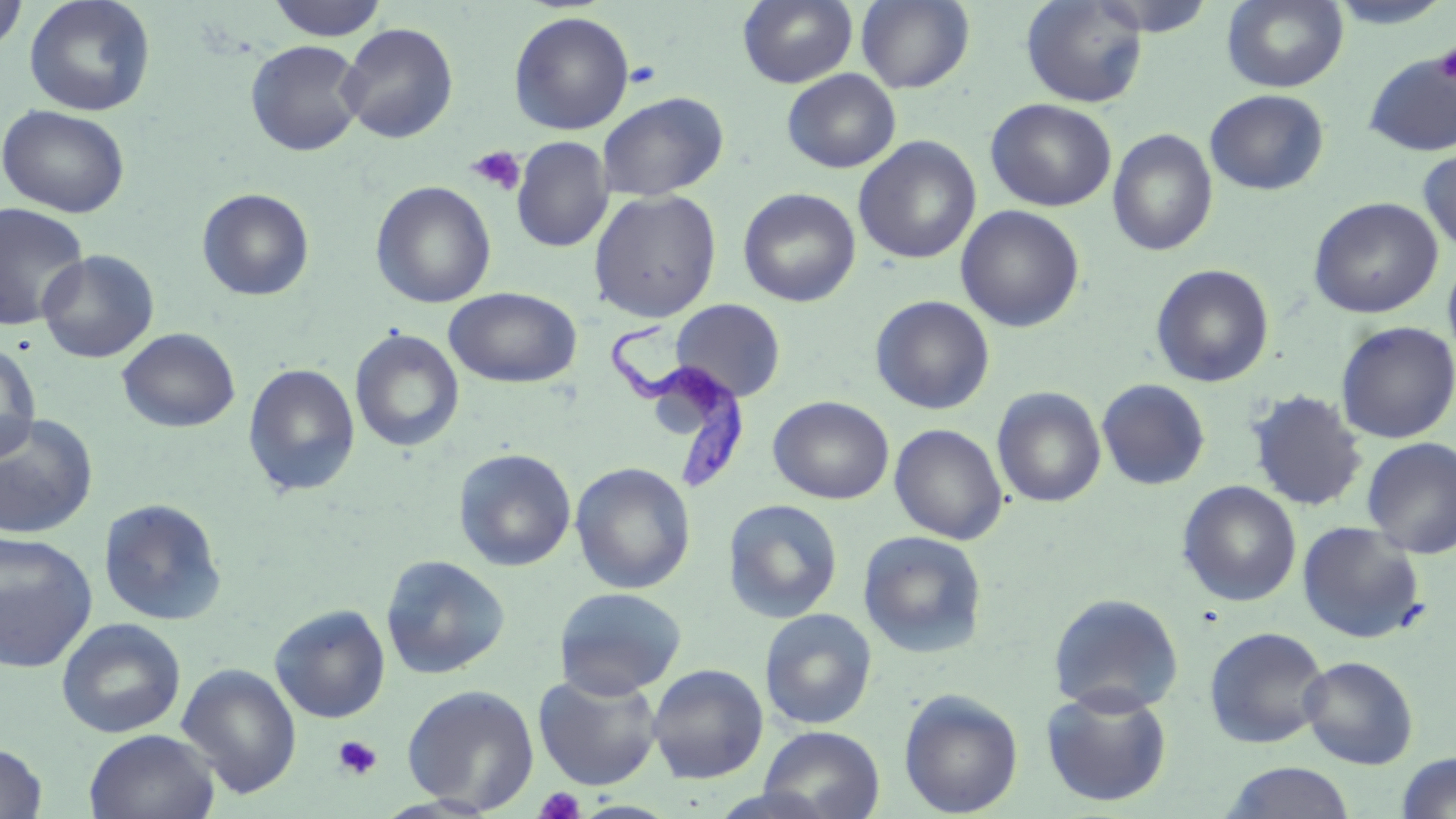
Summary:
  - Coordinate format: approximate bounding boxes as (x1,y1)-(x2,y2) corner pairs in pixels
  - Trypanosoma brucei locations: (602,317)-(748,493)
  - Platelet locations: (1435,44)-(1456,84), (625,60)-(663,89), (466,146)-(527,196), (332,734)-(382,780), (534,787)-(586,818)
  - Uninfected red blood cell locations: (0,0)-(29,54), (24,0)-(156,117), (267,0)-(388,41), (738,0)-(858,88), (856,0)-(975,93), (1222,0)-(1348,92), (1020,1)-(1149,108), (508,11)-(634,135), (338,23)-(459,144), (244,40)-(367,156), (1363,53)-(1456,156), (782,69)-(901,173), (1205,89)-(1329,195), (597,92)-(728,201), (986,98)-(1117,211), (0,104)-(130,218), (1107,128)-(1219,257), (853,136)-(981,265), (512,137)-(612,252), (1417,147)-(1456,255), (370,181)-(496,309), (197,188)-(314,301), (738,188)-(861,307), (588,189)-(722,323), (1308,196)-(1443,318), (0,203)-(90,331), (955,205)-(1085,332), (37,250)-(159,363), (1443,250)-(1456,365), (1151,264)-(1275,388), (444,287)-(582,388), (870,295)-(995,414), (671,298)-(786,402), (1335,321)-(1456,444), (117,328)-(241,433), (349,329)-(465,453), (1,339)-(41,463), (243,363)-(361,498), (1096,378)-(1211,491), (992,387)-(1106,508), (1246,389)-(1368,512), (768,396)-(894,504), (0,413)-(99,540), (889,423)-(1008,545), (1361,437)-(1456,559), (452,447)-(577,572), (570,461)-(696,595), (1176,481)-(1302,607), (97,497)-(227,626), (722,498)-(843,623), (1296,520)-(1426,645), (857,530)-(988,659), (0,531)-(98,672), (380,555)-(510,679), (553,586)-(687,699), (1048,592)-(1184,715), (270,604)-(390,723), (758,608)-(877,729), (56,617)-(186,739), (1203,625)-(1331,749), (1299,655)-(1419,769), (176,663)-(302,798), (647,663)-(769,784), (533,672)-(663,791), (402,684)-(539,814), (1041,687)-(1173,807), (899,688)-(1023,818), (759,725)-(885,819), (84,728)-(220,819), (0,742)-(47,819), (1395,752)-(1456,818), (1219,762)-(1356,819)
  - Slide-level diagnosis: Trypanosoma brucei
  - Modality: light microscopy
  - Magnification: 1000x
  - Field of view: single
  - Image size: 1456×819 pixels
  - Preparation: thin blood film
  - Stain: May-Grünwald-Giemsa